Outline each blood parasite and name the species.
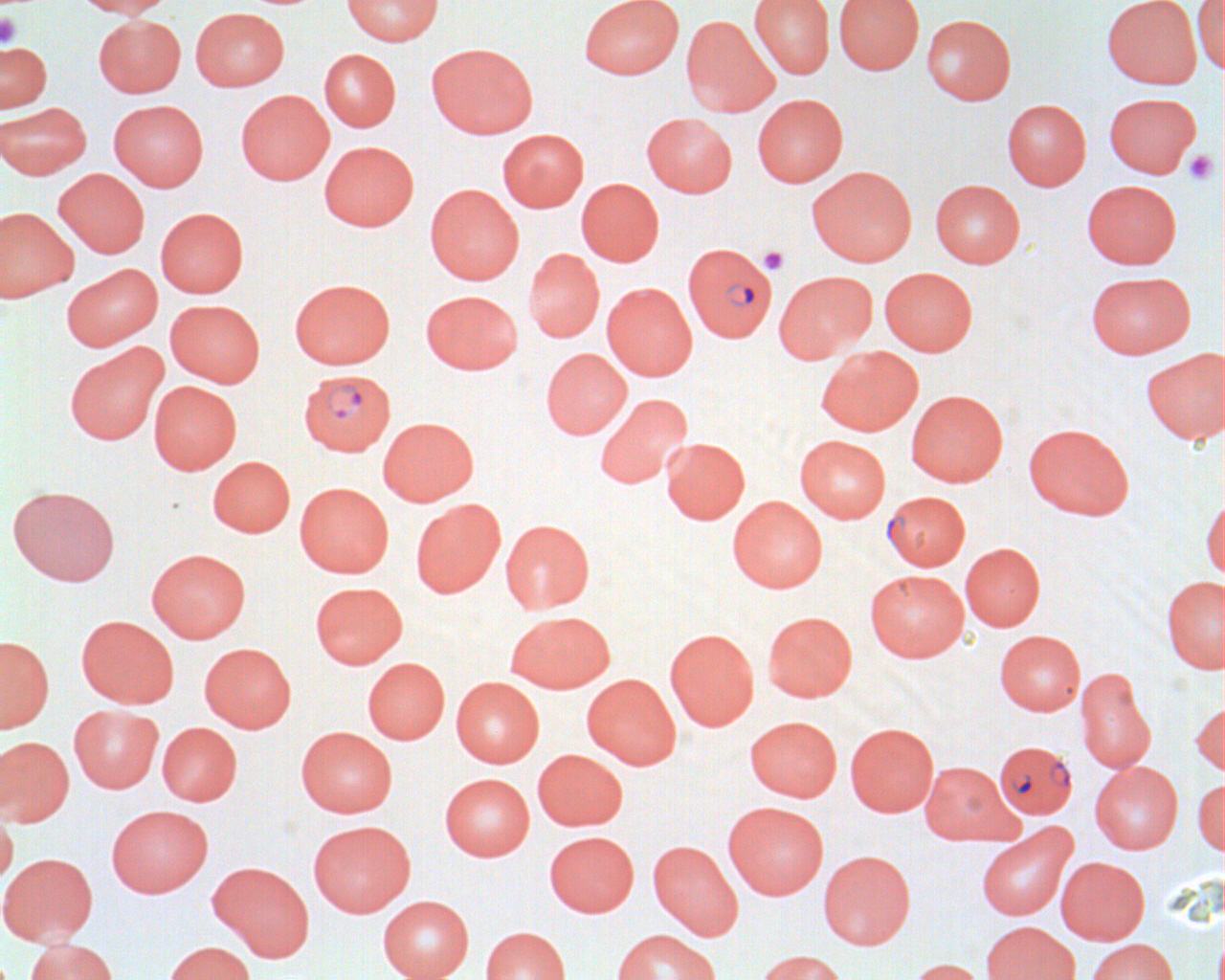

Approximate bounding boxes as named x1/y1/x2/y2 corners in pixels.
Plasmodium falciparum-infected red blood cells: (x1=683, y1=242, x2=776, y2=342), (x1=299, y1=368, x2=396, y2=456), (x1=994, y1=740, x2=1077, y2=818).
No Plasmodium ovale, Plasmodium malariae, Plasmodium vivax, Babesia divergens, or Trypanosoma brucei observed.

Summary:
  - Platelet locations: (x1=0, y1=13, x2=21, y2=48), (x1=1184, y1=149, x2=1218, y2=185), (x1=758, y1=245, x2=788, y2=275)
  - Uninfected red blood cell locations: (x1=71, y1=0, x2=175, y2=18), (x1=341, y1=0, x2=443, y2=46), (x1=579, y1=0, x2=683, y2=79), (x1=749, y1=0, x2=834, y2=79), (x1=833, y1=0, x2=924, y2=74), (x1=1101, y1=0, x2=1202, y2=88), (x1=1192, y1=0, x2=1224, y2=75), (x1=190, y1=7, x2=289, y2=91), (x1=921, y1=14, x2=1016, y2=105), (x1=93, y1=15, x2=186, y2=98), (x1=681, y1=16, x2=779, y2=116), (x1=0, y1=40, x2=52, y2=113), (x1=426, y1=42, x2=538, y2=138), (x1=319, y1=49, x2=401, y2=131), (x1=236, y1=90, x2=334, y2=185), (x1=1103, y1=92, x2=1201, y2=178), (x1=752, y1=94, x2=848, y2=187), (x1=1002, y1=99, x2=1091, y2=190), (x1=108, y1=100, x2=209, y2=191), (x1=0, y1=102, x2=92, y2=179), (x1=642, y1=113, x2=737, y2=197), (x1=497, y1=128, x2=589, y2=211), (x1=319, y1=141, x2=418, y2=231), (x1=807, y1=165, x2=917, y2=266), (x1=53, y1=168, x2=150, y2=258), (x1=577, y1=178, x2=664, y2=266), (x1=930, y1=179, x2=1025, y2=267), (x1=1082, y1=179, x2=1182, y2=268), (x1=426, y1=184, x2=523, y2=284), (x1=0, y1=207, x2=78, y2=303), (x1=156, y1=207, x2=248, y2=297), (x1=523, y1=248, x2=604, y2=343), (x1=61, y1=262, x2=163, y2=351), (x1=879, y1=267, x2=978, y2=355), (x1=774, y1=270, x2=875, y2=363), (x1=1085, y1=271, x2=1195, y2=358), (x1=289, y1=278, x2=395, y2=369), (x1=602, y1=282, x2=697, y2=380), (x1=421, y1=290, x2=523, y2=374), (x1=165, y1=299, x2=265, y2=387), (x1=65, y1=343, x2=168, y2=445), (x1=817, y1=346, x2=923, y2=435), (x1=540, y1=347, x2=631, y2=439), (x1=1141, y1=347, x2=1225, y2=445), (x1=149, y1=380, x2=241, y2=474), (x1=906, y1=390, x2=1008, y2=487), (x1=595, y1=394, x2=692, y2=489), (x1=378, y1=417, x2=478, y2=505), (x1=1023, y1=423, x2=1134, y2=519), (x1=795, y1=435, x2=891, y2=522), (x1=662, y1=438, x2=750, y2=524), (x1=207, y1=456, x2=295, y2=537), (x1=295, y1=482, x2=393, y2=578), (x1=7, y1=485, x2=120, y2=586), (x1=882, y1=491, x2=971, y2=571), (x1=1201, y1=495, x2=1225, y2=582), (x1=728, y1=496, x2=827, y2=592), (x1=410, y1=499, x2=506, y2=597), (x1=501, y1=519, x2=595, y2=613), (x1=960, y1=542, x2=1045, y2=631), (x1=147, y1=548, x2=250, y2=642), (x1=865, y1=569, x2=969, y2=662), (x1=1161, y1=575, x2=1225, y2=673), (x1=309, y1=581, x2=408, y2=668), (x1=505, y1=610, x2=615, y2=693), (x1=763, y1=610, x2=857, y2=702), (x1=76, y1=615, x2=179, y2=708), (x1=665, y1=628, x2=759, y2=730), (x1=994, y1=629, x2=1085, y2=715), (x1=0, y1=635, x2=54, y2=733), (x1=199, y1=643, x2=295, y2=732), (x1=362, y1=657, x2=450, y2=743), (x1=1075, y1=667, x2=1156, y2=773), (x1=582, y1=673, x2=680, y2=769), (x1=451, y1=676, x2=544, y2=767), (x1=1191, y1=699, x2=1225, y2=777), (x1=69, y1=704, x2=163, y2=793), (x1=745, y1=716, x2=842, y2=801), (x1=158, y1=722, x2=241, y2=806), (x1=846, y1=723, x2=938, y2=816), (x1=296, y1=726, x2=397, y2=817), (x1=0, y1=736, x2=74, y2=826), (x1=533, y1=749, x2=627, y2=830), (x1=919, y1=761, x2=1018, y2=845), (x1=1090, y1=761, x2=1183, y2=854), (x1=440, y1=773, x2=535, y2=861), (x1=1192, y1=777, x2=1225, y2=855), (x1=724, y1=801, x2=828, y2=898), (x1=106, y1=804, x2=213, y2=897), (x1=0, y1=808, x2=18, y2=890), (x1=308, y1=820, x2=415, y2=917), (x1=976, y1=823, x2=1076, y2=920), (x1=544, y1=830, x2=639, y2=916), (x1=648, y1=840, x2=743, y2=939), (x1=818, y1=850, x2=915, y2=950), (x1=0, y1=852, x2=98, y2=946), (x1=1056, y1=856, x2=1149, y2=944), (x1=207, y1=861, x2=315, y2=961), (x1=378, y1=895, x2=474, y2=980), (x1=981, y1=920, x2=1080, y2=980), (x1=480, y1=926, x2=571, y2=980), (x1=612, y1=929, x2=721, y2=980), (x1=23, y1=937, x2=119, y2=980), (x1=1086, y1=938, x2=1177, y2=980), (x1=163, y1=941, x2=256, y2=980), (x1=755, y1=949, x2=849, y2=980), (x1=905, y1=957, x2=989, y2=980)
  - Slide-level diagnosis: Plasmodium falciparum
  - Magnification: 1000x
  - Field of view: single
  - Preparation: thin blood smear
  - Modality: light microscopy
  - Image size: 1225×980 pixels